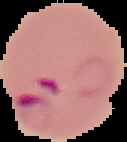 Malaria status: parasitized. From a thin blood smear. The area outside the segmented cell region is set to black. Image is 127×142 pixels.